Assess the morphology of the red blood cells.
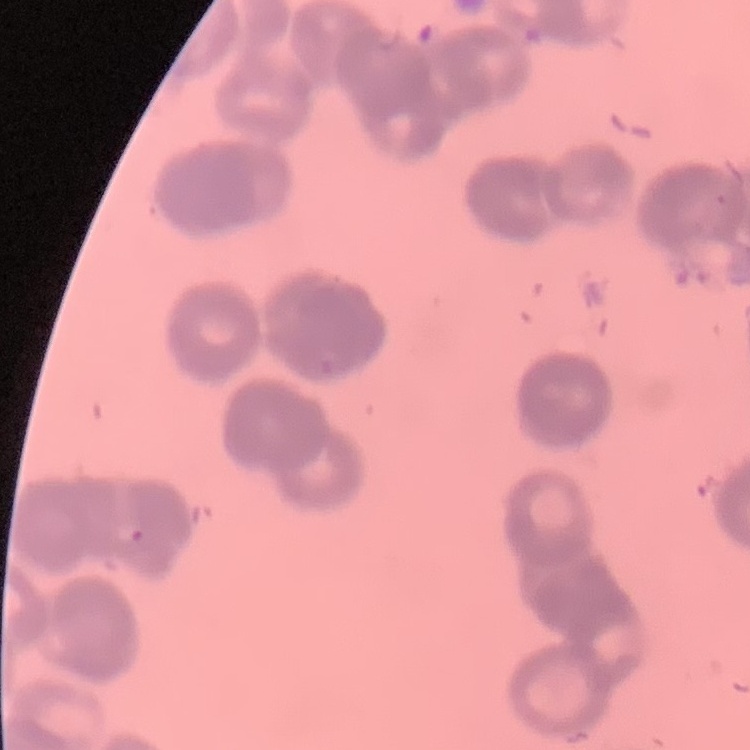
Rouleaux formation.

Summary:
  - Stain: Field's or Giemsa
  - Preparation: thin peripheral smear
  - Image type: square crop of a larger photomicrograph